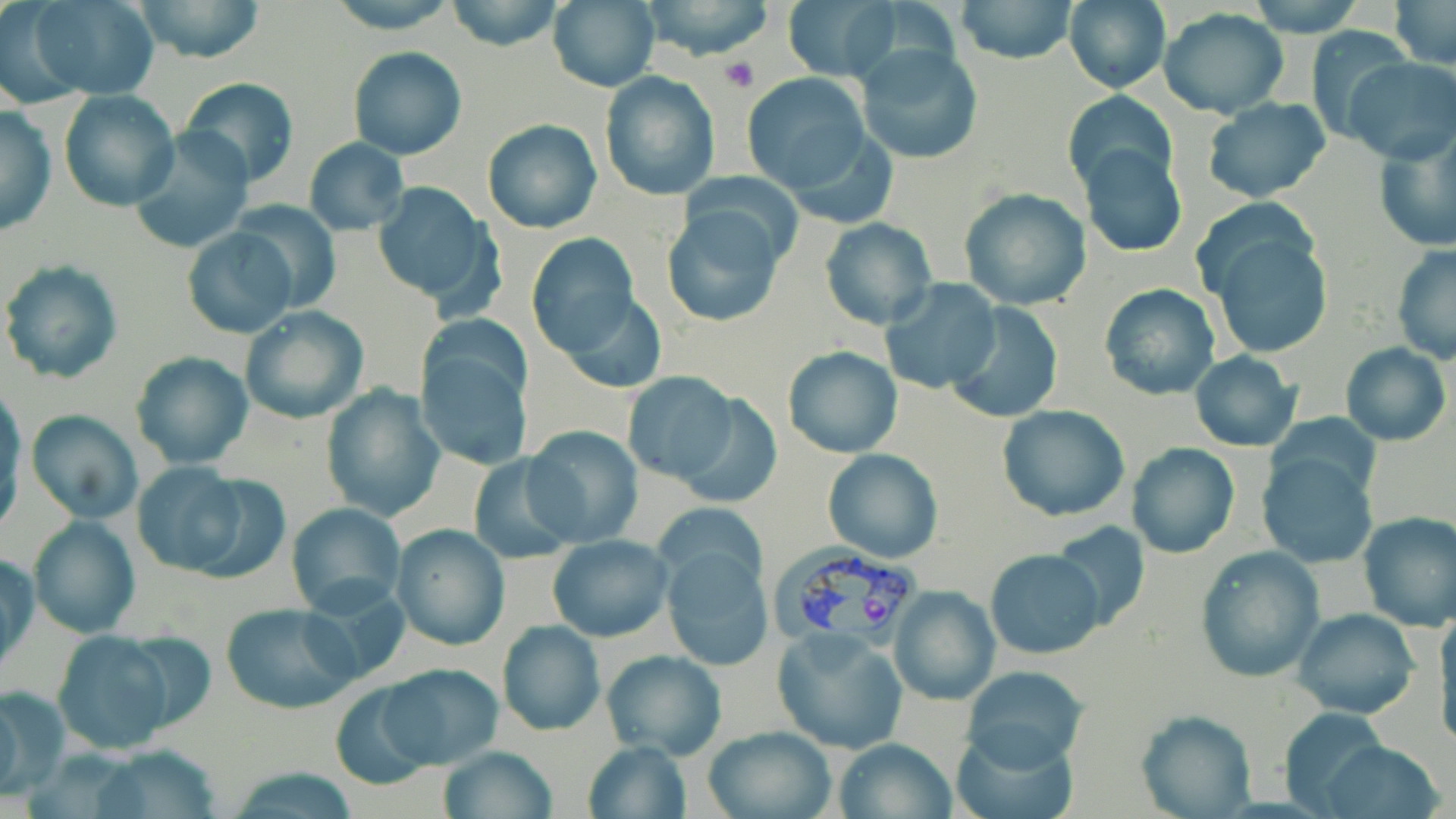

Summary:
  - Coordinate format: approximate bounding boxes as [x1, y1, x2, y2] in pixels
  - Uninfected red blood cell locations: [28, 0, 160, 100], [130, 0, 270, 66], [324, 0, 459, 33], [445, 0, 564, 52], [640, 0, 777, 62], [782, 0, 898, 81], [953, 0, 1078, 65], [1062, 0, 1171, 95], [1243, 0, 1367, 34], [1389, 0, 1455, 68], [548, 1, 658, 91], [1157, 8, 1289, 118], [1303, 26, 1413, 142], [855, 43, 984, 164], [348, 48, 467, 160], [1341, 57, 1456, 163], [600, 72, 720, 200], [740, 73, 872, 195], [178, 76, 300, 188], [1061, 88, 1177, 195], [59, 90, 180, 211], [1200, 97, 1331, 203], [1, 103, 55, 236], [482, 119, 603, 234], [1372, 123, 1456, 253], [131, 128, 257, 253], [303, 139, 408, 236], [1078, 143, 1187, 257], [683, 170, 805, 269], [372, 184, 503, 315], [957, 188, 1092, 311], [227, 198, 343, 315], [664, 207, 785, 326], [818, 217, 938, 330], [1199, 222, 1334, 360], [182, 227, 297, 339], [525, 234, 639, 356], [1391, 246, 1456, 364], [3, 260, 123, 386], [881, 279, 1002, 395], [1098, 284, 1221, 400], [555, 291, 668, 395], [947, 303, 1063, 423], [240, 307, 368, 424], [413, 323, 537, 471], [1340, 343, 1451, 445], [783, 345, 902, 458], [130, 351, 254, 469], [1188, 351, 1302, 451], [622, 372, 740, 483], [321, 385, 443, 523], [675, 393, 785, 509], [1, 396, 23, 531], [996, 405, 1131, 520], [24, 411, 144, 523], [524, 426, 644, 549], [1126, 441, 1240, 559], [1257, 448, 1380, 568], [824, 449, 943, 562], [467, 453, 580, 564], [131, 462, 249, 574], [285, 502, 405, 616], [1356, 509, 1456, 632], [26, 515, 140, 639], [1051, 522, 1151, 632], [390, 524, 509, 650], [546, 535, 672, 641], [662, 543, 773, 671], [1195, 547, 1326, 682], [986, 548, 1104, 661], [1, 551, 39, 675], [301, 579, 413, 692], [888, 585, 1000, 705], [221, 600, 359, 714], [1291, 607, 1421, 721], [1433, 612, 1456, 748], [497, 620, 604, 736], [771, 627, 907, 754], [50, 630, 181, 755], [601, 648, 726, 761], [377, 663, 504, 770], [961, 665, 1090, 771], [328, 680, 441, 792], [0, 684, 70, 798], [1276, 706, 1391, 812], [1134, 709, 1257, 819], [702, 725, 839, 819], [947, 727, 1079, 819], [833, 737, 956, 818], [581, 740, 692, 819], [1317, 741, 1445, 819], [93, 746, 227, 818], [436, 746, 556, 819]
  - Platelet locations: [721, 58, 758, 92]
  - Plasmodium vivax-infected red blood cell locations: [772, 540, 921, 673]
  - Slide-level diagnosis: Plasmodium vivax
  - Magnification: 1000x
  - Image size: 1456×819 pixels
  - Preparation: thin blood film
  - Stain: May-Grünwald-Giemsa
  - Modality: optical microscopy
  - Field of view: single